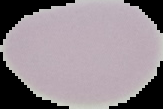

malaria status = uninfected
image size = 163×109 pixels
preparation = thin blood film
image type = cell region segmented out of the field of view; surrounding area masked to black